Classify this cell by malaria status.
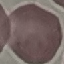

Uninfected.

{
  "stain": "Giemsa",
  "image_type": "cell patch, automatically extracted from a larger field of view and resized to 64 × 64 pixels",
  "capture": "smartphone camera at the microscope eyepiece",
  "preparation": "thin smear"
}